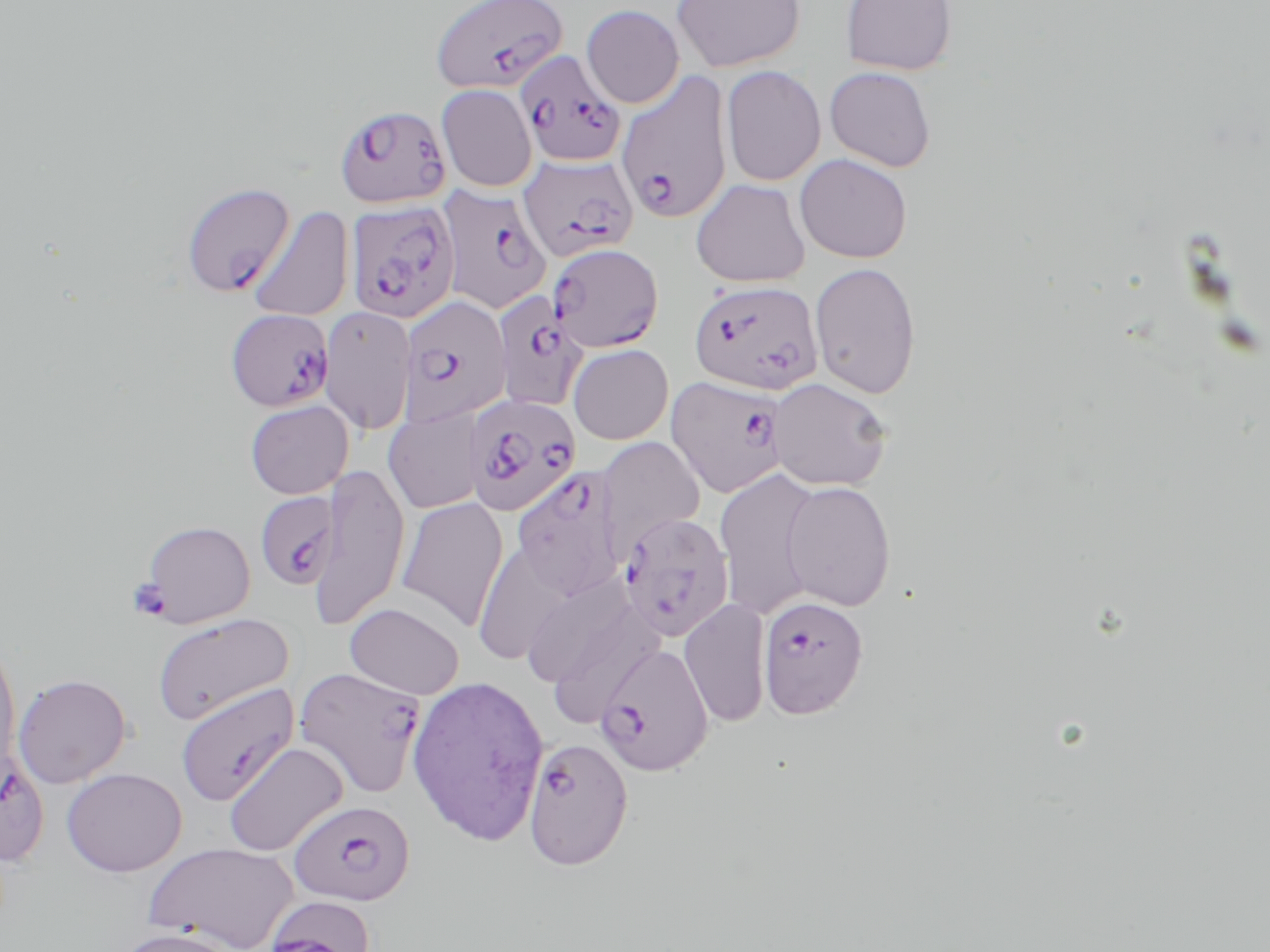 Approximate bounding boxes as (x1, y1, x2, y2) in pixels. Uninfected red blood cell locations (subset): (671, 0, 805, 73), (839, 0, 958, 76), (580, 4, 684, 108), (721, 65, 826, 187), (824, 66, 937, 172), (435, 84, 537, 192), (794, 153, 913, 263), (691, 178, 810, 287), (247, 206, 354, 322), (809, 261, 922, 399), (318, 304, 417, 435), (567, 343, 674, 444), (768, 377, 894, 491), (245, 399, 354, 499), (383, 409, 484, 513), (595, 436, 706, 556), (309, 460, 410, 630), (714, 467, 823, 620), (781, 480, 897, 611), (394, 497, 509, 631), (139, 520, 256, 627), (472, 540, 578, 667), (525, 574, 661, 710), (679, 598, 771, 728), (345, 602, 465, 699), (151, 612, 293, 725), (0, 635, 22, 778), (12, 672, 132, 789), (406, 673, 550, 846), (174, 682, 299, 805), (222, 741, 348, 856), (62, 767, 187, 877), (143, 841, 300, 951), (110, 925, 245, 952). Plasmodium falciparum-infected red blood cell locations (subset): (430, 0, 569, 94), (516, 50, 626, 167), (616, 71, 733, 225), (334, 103, 451, 209), (518, 153, 639, 263), (180, 181, 295, 297), (437, 185, 553, 315), (345, 200, 460, 324), (547, 242, 664, 352), (689, 279, 823, 395), (491, 291, 588, 413), (397, 294, 512, 428), (225, 308, 334, 411), (665, 375, 789, 499), (464, 393, 582, 516), (510, 466, 627, 600), (254, 490, 340, 591), (617, 511, 735, 642), (757, 594, 869, 719), (595, 642, 714, 776), (294, 665, 427, 799), (0, 744, 49, 867), (288, 798, 415, 907), (263, 896, 377, 952). Platelet locations: (126, 577, 172, 621). Slide-level diagnosis: Plasmodium falciparum. Image is 1270×952 pixels. Thin blood film. Light microscopy. One field of a larger specimen. May-Grünwald-Giemsa stain. 1000x magnification.